Assess this cell for malaria.
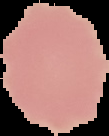

Uninfected.

image_size: 109×136 pixels
preparation: thin blood smear
image_type: segmented cell region with the area outside set to black